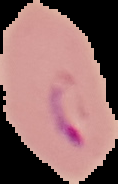

From a thin blood smear. Image is 118×184 pixels. Malaria status: parasitized. Segmented cell region on a black background.